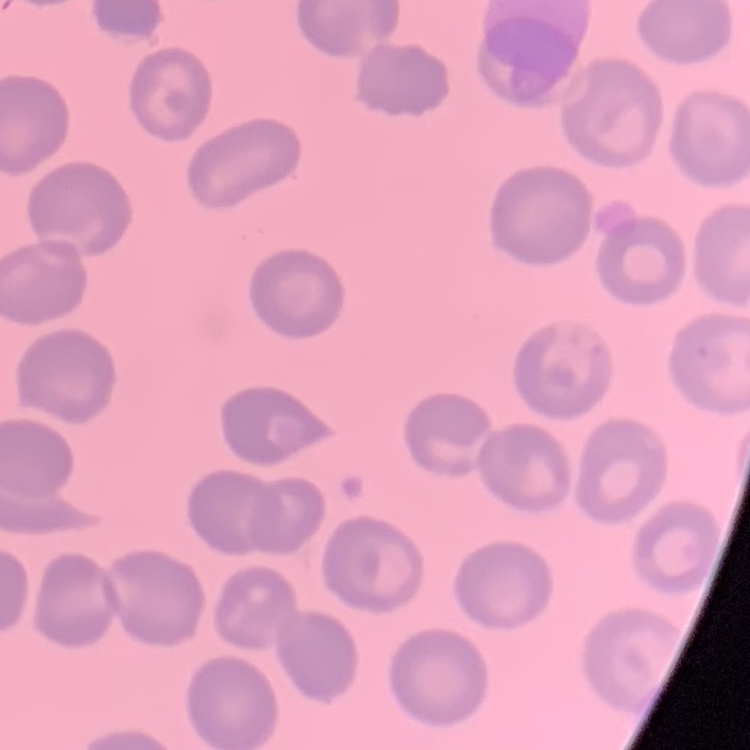

erythrocyte morphology = no rouleaux formation
image type = one tile cut from a larger photomicrograph
stain = Field's or Giemsa
preparation = thin peripheral smear